Report the malaria status of this cell.
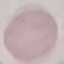
It is uninfected.

Thin blood smear. Automatically extracted cell patch, resized to 64 × 64 pixels. Photographed with a smartphone camera at the microscope eyepiece. Giemsa stain.